Assess this cell for malaria.
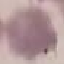
Uninfected.

Automatically extracted cell patch, resized to 64 × 64 pixels. Giemsa-stained preparation. Acquired by smartphone through the microscope eyepiece. Thin smear of blood.